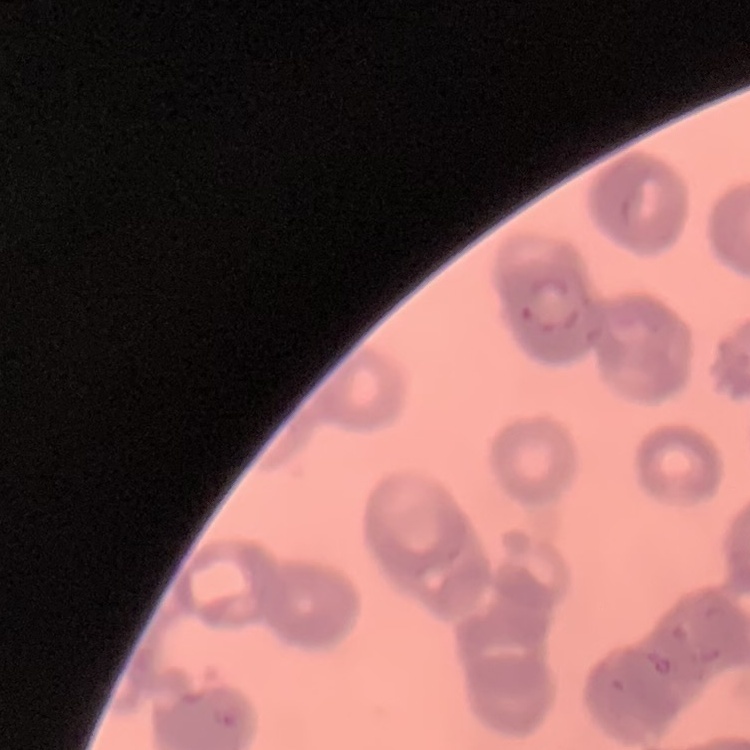

Summary:
  - Red blood cell morphology: rouleaux formation
  - Stain: Field's or Giemsa
  - Preparation: thin blood smear
  - Image type: square crop of a larger photomicrograph